Outline each blood parasite and name the species.
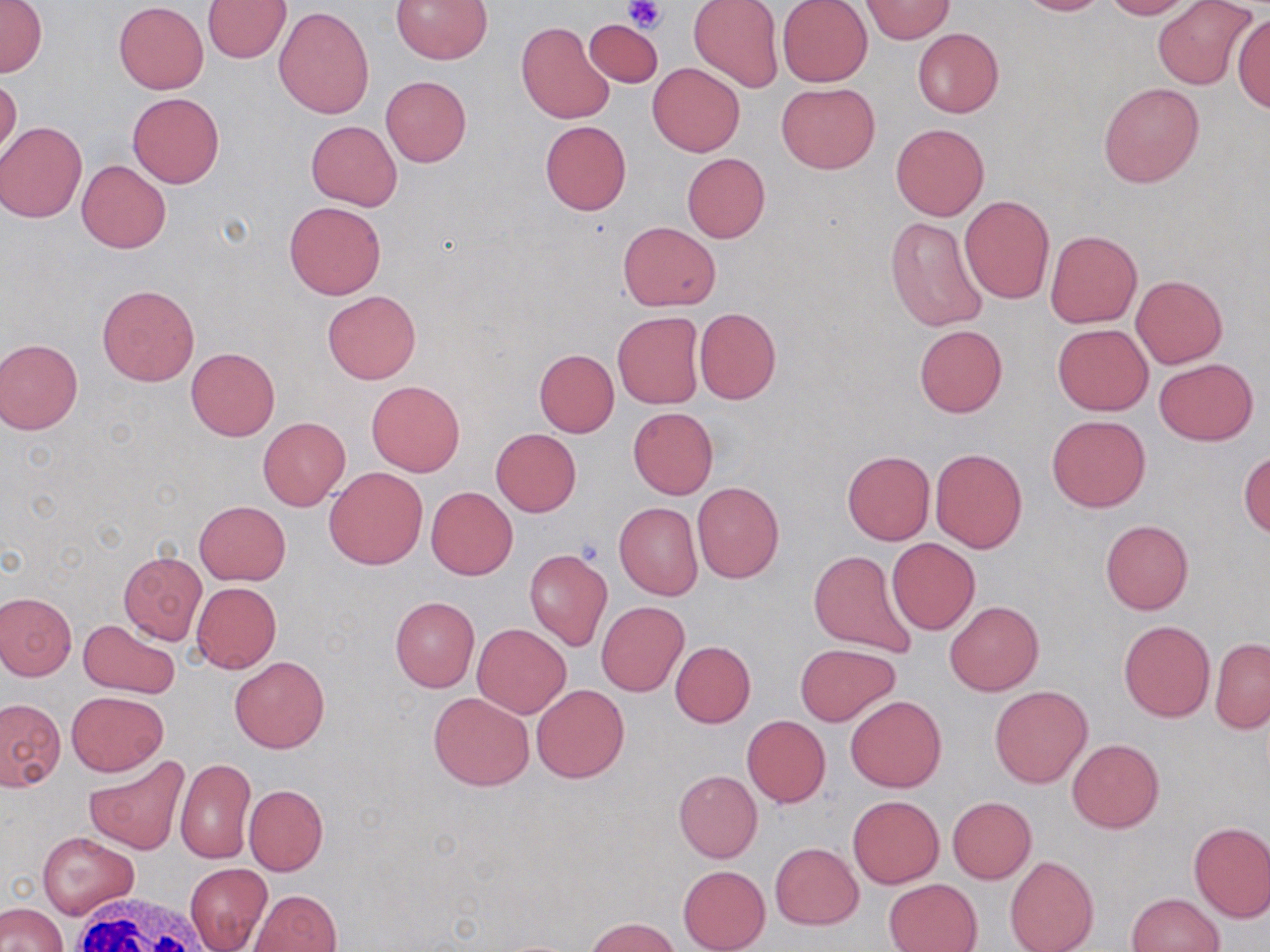

No blood parasites observed.

{
  "slide_level_diagnosis": "negative for blood parasites",
  "magnification": "1000x",
  "preparation": "thin blood film",
  "white_blood_cell_locations": "approximate bounding boxes as [x1, y1, x2, y2] in pixels: [61, 891, 219, 952]",
  "field_of_view": "single",
  "modality": "optical microscopy",
  "platelet_locations": "approximate bounding boxes as [x1, y1, x2, y2] in pixels: [624, 0, 666, 33]",
  "uninfected_red_blood_cell_locations": "approximate bounding boxes as [x1, y1, x2, y2] in pixels: [391, 0, 492, 65], [1016, 0, 1110, 16], [1102, 0, 1193, 19], [1152, 0, 1256, 89], [0, 1, 46, 77], [202, 1, 290, 63], [689, 1, 784, 92], [777, 1, 872, 87], [861, 1, 954, 43], [114, 2, 208, 93], [274, 6, 375, 117], [1232, 14, 1269, 115], [584, 19, 663, 86], [517, 21, 615, 123], [912, 27, 1003, 118], [648, 62, 745, 156], [0, 74, 21, 161], [381, 76, 471, 167], [1098, 80, 1205, 188], [776, 82, 879, 174], [127, 92, 225, 188], [306, 120, 403, 211], [540, 121, 631, 215], [0, 122, 87, 223], [891, 123, 989, 220], [682, 152, 770, 242], [77, 160, 170, 253], [959, 197, 1054, 303], [284, 201, 386, 299], [886, 218, 987, 331], [618, 221, 719, 311], [1044, 230, 1142, 328], [1131, 274, 1227, 368], [97, 283, 200, 386], [323, 290, 421, 383], [694, 307, 781, 403], [613, 311, 705, 409], [914, 323, 1007, 417], [1052, 323, 1152, 415], [0, 337, 84, 434], [186, 348, 280, 440], [534, 348, 619, 437], [1153, 358, 1258, 445], [367, 380, 465, 476], [628, 407, 718, 499], [1047, 415, 1151, 512], [258, 417, 349, 510], [490, 428, 582, 517], [931, 448, 1027, 552], [1239, 449, 1269, 539], [842, 450, 935, 545], [324, 466, 428, 570], [692, 481, 783, 583], [426, 486, 517, 580], [195, 501, 289, 583], [614, 502, 703, 600], [1100, 520, 1194, 614], [887, 538, 980, 635], [807, 549, 918, 659], [119, 551, 206, 644], [523, 551, 611, 651], [804, 581, 909, 715], [191, 582, 281, 673], [0, 592, 76, 679], [389, 595, 479, 692], [944, 601, 1044, 695], [596, 602, 689, 696], [79, 618, 180, 699], [1119, 620, 1215, 721], [472, 622, 571, 717], [1210, 639, 1270, 733], [670, 641, 756, 727], [795, 643, 899, 726], [231, 655, 329, 753], [531, 683, 630, 782], [989, 685, 1092, 787], [66, 691, 168, 775], [428, 691, 535, 790], [845, 695, 947, 792], [0, 698, 65, 790], [741, 716, 830, 808], [1066, 739, 1164, 833], [84, 754, 190, 854], [176, 758, 255, 864], [674, 770, 762, 862], [243, 784, 328, 875], [847, 795, 944, 888], [946, 796, 1036, 884], [1188, 821, 1270, 922], [38, 833, 140, 918], [770, 843, 864, 929], [1005, 854, 1098, 952], [185, 864, 272, 951], [678, 865, 771, 952], [885, 879, 980, 952], [250, 889, 342, 952], [1127, 892, 1225, 952], [0, 903, 68, 952], [588, 917, 681, 952]",
  "image_size": "1270×952 pixels",
  "stain": "May-Grünwald-Giemsa"
}